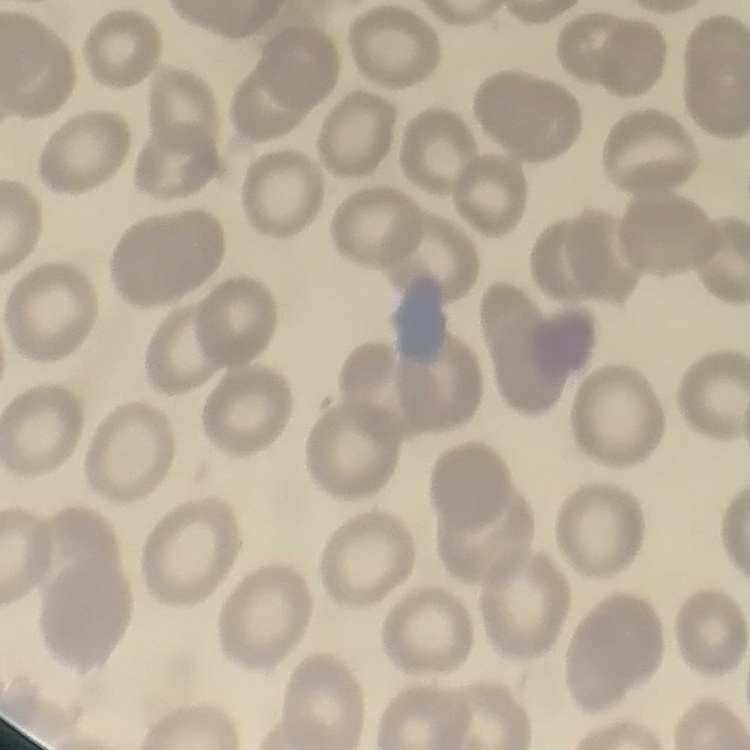

The red blood cells exhibit no rouleaux formation. Stained with either Field's or Giemsa. Thin blood smear. One tile cut from a larger photomicrograph.